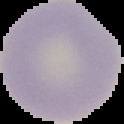

Malaria status: uninfected. Cell region segmented out of the field of view; the surrounding area is masked to black. Image is 124×124 pixels. From a thin blood smear.